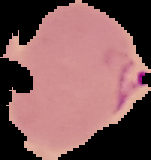
image type = cell region segmented out of the field of view; surrounding area masked to black
malaria status = parasitized
image size = 151×160 pixels
preparation = thin blood film